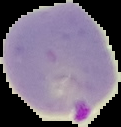

{
  "malaria_status": "parasitized",
  "image_type": "cell region segmented out of the field of view; surrounding area masked to black",
  "preparation": "thin blood film",
  "image_size": "121×127 pixels"
}